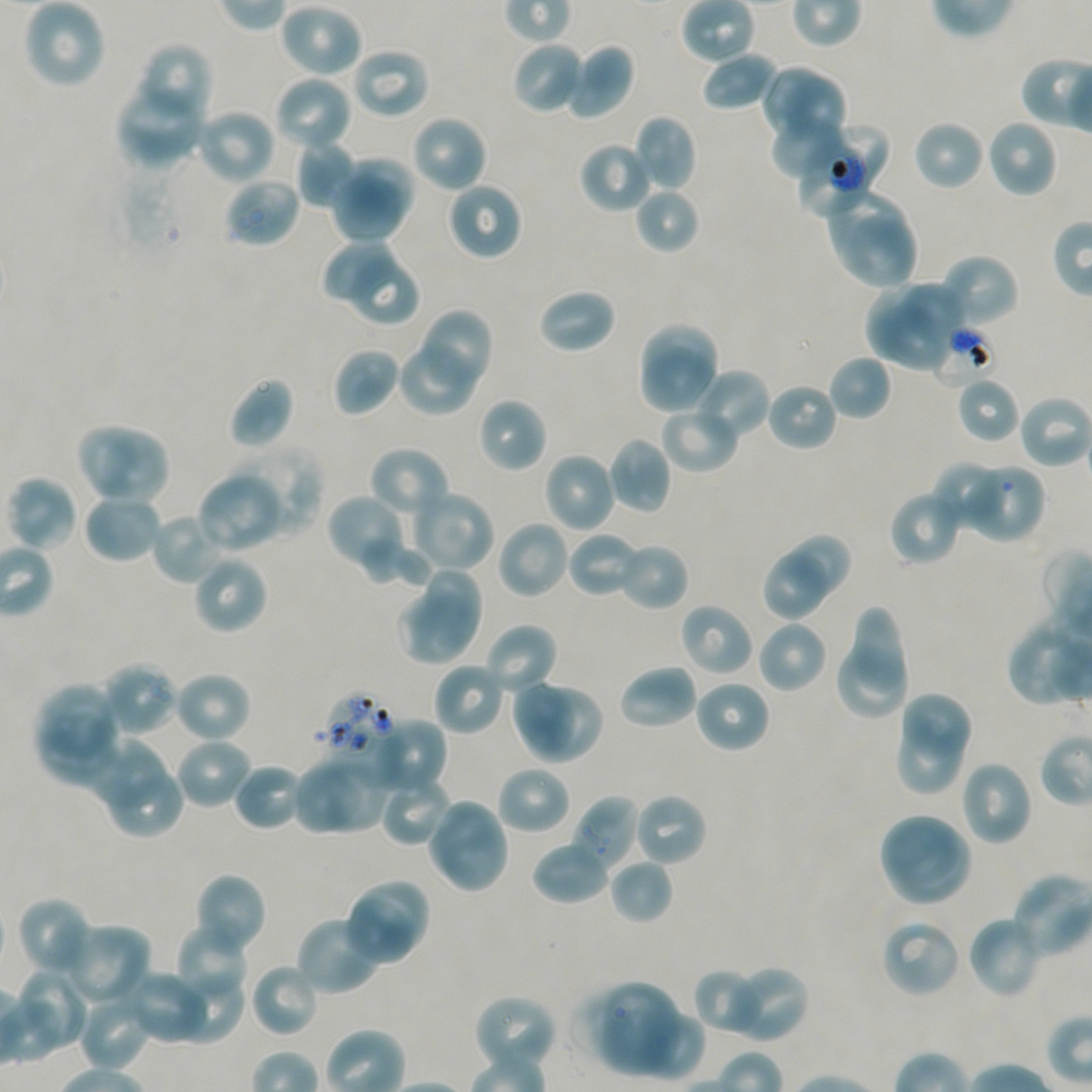

Approximate bounding boxes as (x1, y1, x2, y2) in pixels. Not every red blood cell is marked.
Summary:
  - Locations of red blood cells of indeterminate infection status: (797, 124, 888, 217), (930, 323, 996, 388), (322, 691, 398, 766), (571, 795, 640, 875)
  - Locations of uninfected red blood cells: (22, 0, 106, 89), (278, 4, 363, 79), (511, 41, 585, 115), (138, 43, 213, 124), (565, 43, 636, 121), (350, 47, 431, 120), (702, 51, 780, 113), (761, 65, 822, 143), (784, 71, 849, 151), (273, 75, 353, 153), (115, 81, 205, 170), (196, 108, 275, 185), (411, 114, 488, 194), (632, 114, 698, 192), (769, 115, 847, 179), (985, 119, 1058, 198), (913, 120, 985, 192), (295, 139, 357, 207), (578, 140, 655, 214), (342, 158, 418, 224), (331, 175, 403, 245), (225, 176, 301, 249), (445, 181, 523, 261), (634, 186, 700, 254), (824, 187, 911, 264), (840, 216, 920, 290), (323, 241, 395, 298), (937, 253, 1020, 328), (349, 256, 421, 326), (865, 276, 933, 361), (904, 282, 966, 341), (536, 287, 617, 355), (880, 304, 949, 371), (416, 308, 493, 392), (640, 323, 719, 388), (397, 338, 478, 417), (333, 347, 401, 417), (638, 350, 721, 416), (828, 354, 892, 421), (691, 367, 771, 442), (228, 376, 294, 450), (956, 376, 1021, 443), (765, 381, 839, 452), (1017, 394, 1092, 469), (477, 397, 548, 473), (659, 405, 740, 473), (75, 422, 138, 495), (101, 429, 170, 502), (606, 437, 672, 514), (369, 445, 451, 522), (228, 446, 323, 539), (543, 452, 618, 534), (931, 461, 1007, 534), (964, 463, 1044, 543), (196, 470, 285, 553), (6, 475, 78, 552), (889, 488, 965, 566), (412, 490, 496, 572), (82, 491, 163, 564), (326, 493, 406, 573), (150, 511, 228, 585), (496, 520, 570, 600), (567, 531, 642, 598), (789, 534, 851, 597), (362, 536, 434, 587), (617, 542, 689, 611), (192, 554, 269, 635), (765, 554, 826, 620), (422, 566, 484, 647), (396, 594, 471, 661), (678, 601, 755, 678), (850, 611, 909, 691), (1006, 615, 1092, 708), (756, 619, 828, 694), (483, 623, 559, 699), (839, 647, 908, 718), (100, 661, 179, 736), (433, 662, 506, 736), (617, 664, 699, 731), (172, 670, 253, 743), (693, 678, 771, 754), (511, 679, 577, 757), (34, 683, 114, 755), (530, 688, 604, 763), (900, 691, 972, 762), (40, 710, 120, 784), (368, 717, 447, 796), (894, 726, 963, 795), (174, 737, 255, 810), (79, 738, 166, 809), (323, 757, 386, 832), (960, 759, 1034, 847), (232, 762, 304, 831), (291, 763, 362, 833), (496, 764, 572, 835), (379, 774, 454, 847), (111, 777, 186, 839), (632, 792, 708, 867), (425, 797, 511, 895), (877, 812, 962, 888), (891, 833, 971, 904), (530, 839, 613, 905), (610, 858, 673, 924), (193, 873, 268, 957), (1009, 873, 1092, 959), (359, 880, 432, 949), (342, 892, 417, 966), (17, 896, 94, 978), (295, 913, 384, 996), (966, 914, 1043, 999), (880, 918, 962, 998), (61, 922, 152, 1008), (175, 922, 250, 1003), (249, 962, 320, 1038), (725, 964, 809, 1043), (19, 968, 92, 1048), (170, 968, 244, 1044), (692, 968, 765, 1036), (124, 969, 211, 1044), (45, 979, 136, 1069), (591, 981, 682, 1076), (77, 994, 151, 1072), (473, 994, 558, 1072), (641, 1011, 706, 1081)
  - Donor blood group: A+/O+
  - Field of view: single
  - Image size: 1092×1092 pixels
  - Objective: 100x, oil immersion, numerical aperture 1.45
  - Preparation: thin blood film
  - Culture: static in-vitro Plasmodium falciparum strain NF54
  - Stain: Giemsa